Name the blood parasite species.
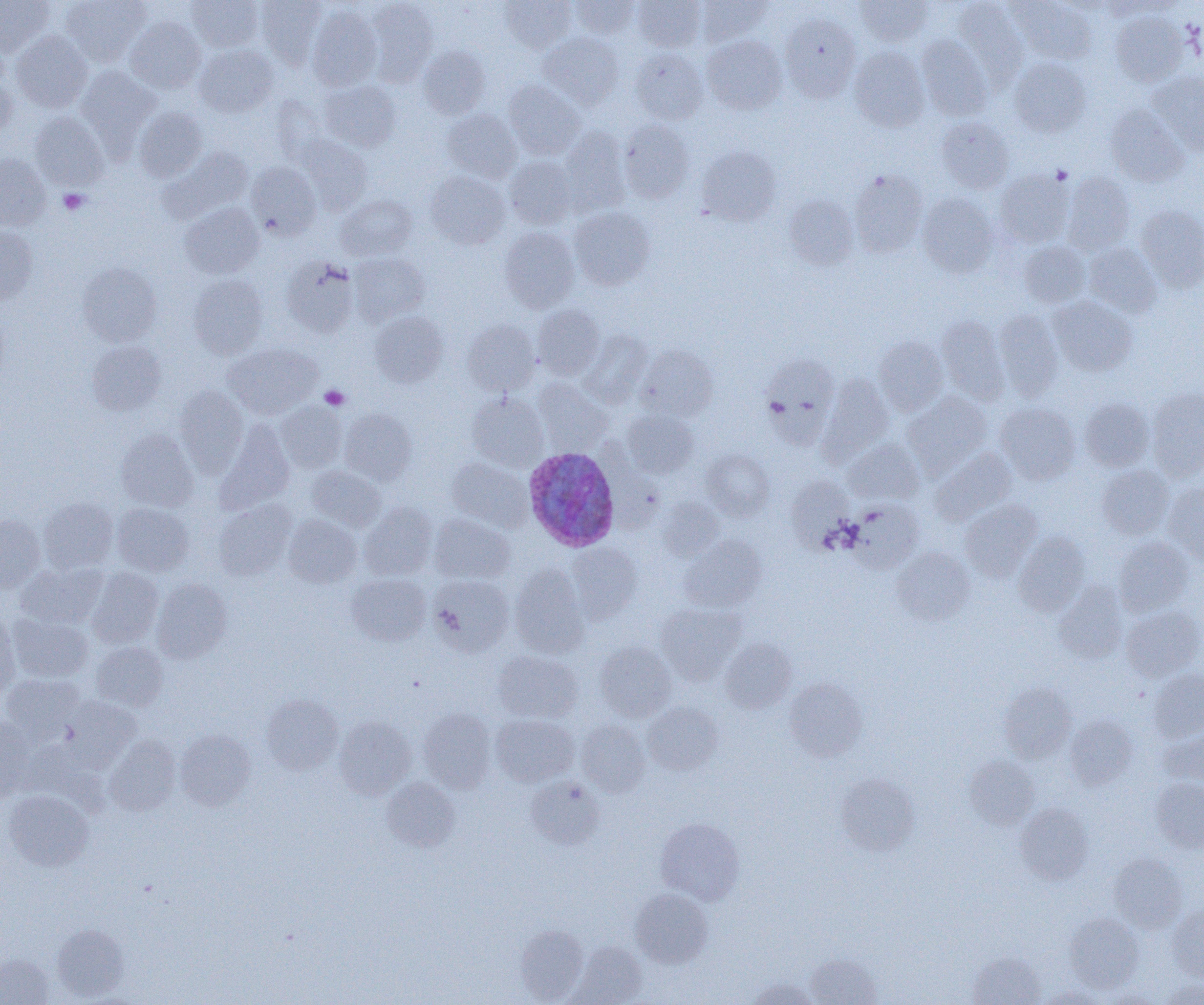
Plasmodium ovale.

Approximate bounding boxes as named x1/y1/x2/y2 corners in pixels. Platelet locations: (x1=59, y1=188, x2=89, y2=214), (x1=320, y1=385, x2=349, y2=410). Plasmodium ovale-infected red blood cell locations: (x1=523, y1=446, x2=620, y2=552). Uninfected red blood cell locations: (x1=0, y1=0, x2=54, y2=56), (x1=61, y1=0, x2=149, y2=65), (x1=187, y1=0, x2=263, y2=51), (x1=256, y1=0, x2=326, y2=69), (x1=366, y1=0, x2=438, y2=83), (x1=569, y1=0, x2=640, y2=39), (x1=632, y1=0, x2=705, y2=52), (x1=696, y1=0, x2=771, y2=46), (x1=856, y1=0, x2=931, y2=46), (x1=500, y1=1, x2=575, y2=52), (x1=954, y1=1, x2=1028, y2=86), (x1=1008, y1=1, x2=1096, y2=64), (x1=307, y1=5, x2=383, y2=91), (x1=1112, y1=11, x2=1189, y2=86), (x1=780, y1=14, x2=861, y2=102), (x1=125, y1=17, x2=206, y2=93), (x1=11, y1=30, x2=92, y2=112), (x1=539, y1=32, x2=623, y2=108), (x1=702, y1=35, x2=787, y2=114), (x1=916, y1=35, x2=992, y2=120), (x1=194, y1=44, x2=278, y2=117), (x1=418, y1=45, x2=490, y2=119), (x1=849, y1=47, x2=929, y2=132), (x1=630, y1=48, x2=708, y2=124), (x1=1009, y1=57, x2=1091, y2=137), (x1=76, y1=66, x2=160, y2=149), (x1=1147, y1=72, x2=1204, y2=156), (x1=0, y1=73, x2=17, y2=141), (x1=320, y1=80, x2=402, y2=151), (x1=503, y1=81, x2=586, y2=159), (x1=272, y1=95, x2=331, y2=166), (x1=1106, y1=105, x2=1189, y2=186), (x1=134, y1=107, x2=207, y2=181), (x1=443, y1=109, x2=521, y2=182), (x1=30, y1=112, x2=109, y2=190), (x1=936, y1=117, x2=1013, y2=193), (x1=619, y1=120, x2=694, y2=203), (x1=560, y1=127, x2=629, y2=214), (x1=296, y1=136, x2=372, y2=214), (x1=162, y1=146, x2=254, y2=223), (x1=696, y1=146, x2=780, y2=226), (x1=0, y1=154, x2=50, y2=231), (x1=505, y1=156, x2=578, y2=228), (x1=247, y1=162, x2=321, y2=239), (x1=849, y1=170, x2=927, y2=257), (x1=995, y1=170, x2=1074, y2=247), (x1=425, y1=171, x2=510, y2=249), (x1=1062, y1=172, x2=1135, y2=254), (x1=337, y1=194, x2=417, y2=260), (x1=918, y1=194, x2=998, y2=277), (x1=784, y1=195, x2=858, y2=270), (x1=181, y1=202, x2=264, y2=279), (x1=1136, y1=204, x2=1204, y2=291), (x1=569, y1=207, x2=655, y2=290), (x1=0, y1=226, x2=37, y2=304), (x1=499, y1=227, x2=579, y2=312), (x1=1019, y1=241, x2=1090, y2=309), (x1=1083, y1=243, x2=1162, y2=317), (x1=349, y1=253, x2=429, y2=325), (x1=280, y1=256, x2=359, y2=337), (x1=78, y1=262, x2=162, y2=346), (x1=188, y1=275, x2=267, y2=359), (x1=1049, y1=296, x2=1137, y2=376), (x1=533, y1=304, x2=605, y2=379), (x1=994, y1=310, x2=1063, y2=400), (x1=370, y1=311, x2=448, y2=387), (x1=937, y1=316, x2=1008, y2=402), (x1=462, y1=320, x2=541, y2=395), (x1=580, y1=330, x2=652, y2=408), (x1=873, y1=336, x2=948, y2=415), (x1=86, y1=340, x2=166, y2=415), (x1=223, y1=343, x2=322, y2=418), (x1=637, y1=345, x2=718, y2=421), (x1=762, y1=354, x2=840, y2=445), (x1=819, y1=375, x2=893, y2=461), (x1=534, y1=379, x2=611, y2=454), (x1=174, y1=386, x2=248, y2=475), (x1=1147, y1=389, x2=1204, y2=480), (x1=467, y1=392, x2=549, y2=471), (x1=904, y1=392, x2=992, y2=474), (x1=1080, y1=398, x2=1154, y2=471), (x1=276, y1=402, x2=347, y2=472), (x1=995, y1=403, x2=1081, y2=484), (x1=340, y1=408, x2=416, y2=485), (x1=622, y1=410, x2=698, y2=478), (x1=215, y1=422, x2=295, y2=513), (x1=116, y1=429, x2=198, y2=512), (x1=843, y1=439, x2=923, y2=504), (x1=931, y1=448, x2=1016, y2=526), (x1=702, y1=449, x2=774, y2=519), (x1=447, y1=458, x2=532, y2=531), (x1=1097, y1=465, x2=1174, y2=539), (x1=306, y1=466, x2=386, y2=531), (x1=786, y1=475, x2=851, y2=547), (x1=1164, y1=484, x2=1204, y2=565), (x1=38, y1=497, x2=118, y2=573), (x1=658, y1=497, x2=724, y2=561), (x1=214, y1=500, x2=297, y2=580), (x1=848, y1=500, x2=923, y2=571), (x1=961, y1=500, x2=1042, y2=581), (x1=360, y1=502, x2=437, y2=579), (x1=112, y1=503, x2=194, y2=575), (x1=284, y1=514, x2=362, y2=587), (x1=430, y1=514, x2=514, y2=584), (x1=0, y1=515, x2=46, y2=593), (x1=1013, y1=532, x2=1090, y2=616), (x1=680, y1=536, x2=766, y2=612), (x1=1114, y1=536, x2=1194, y2=616), (x1=568, y1=543, x2=642, y2=621), (x1=893, y1=547, x2=975, y2=625), (x1=16, y1=562, x2=109, y2=629), (x1=510, y1=565, x2=589, y2=656), (x1=86, y1=568, x2=163, y2=648), (x1=347, y1=573, x2=430, y2=646), (x1=430, y1=575, x2=513, y2=655), (x1=151, y1=578, x2=231, y2=662), (x1=1054, y1=582, x2=1127, y2=663), (x1=657, y1=602, x2=744, y2=683), (x1=1121, y1=605, x2=1204, y2=681), (x1=0, y1=612, x2=20, y2=698), (x1=7, y1=613, x2=93, y2=682), (x1=720, y1=638, x2=796, y2=713), (x1=91, y1=642, x2=168, y2=711), (x1=596, y1=642, x2=675, y2=721), (x1=492, y1=650, x2=582, y2=723), (x1=1148, y1=669, x2=1204, y2=741), (x1=1, y1=673, x2=85, y2=742), (x1=785, y1=678, x2=867, y2=761), (x1=999, y1=683, x2=1076, y2=762), (x1=261, y1=695, x2=343, y2=775), (x1=61, y1=696, x2=141, y2=771), (x1=643, y1=702, x2=723, y2=775), (x1=418, y1=708, x2=496, y2=792), (x1=491, y1=714, x2=578, y2=787), (x1=1065, y1=714, x2=1138, y2=789), (x1=0, y1=715, x2=36, y2=800), (x1=334, y1=717, x2=416, y2=800), (x1=576, y1=720, x2=650, y2=796), (x1=1159, y1=728, x2=1204, y2=787), (x1=175, y1=729, x2=256, y2=810), (x1=104, y1=736, x2=181, y2=815), (x1=964, y1=756, x2=1039, y2=829), (x1=835, y1=774, x2=919, y2=855), (x1=525, y1=776, x2=604, y2=849), (x1=382, y1=778, x2=460, y2=851), (x1=1150, y1=778, x2=1204, y2=852), (x1=3, y1=790, x2=94, y2=871), (x1=1016, y1=804, x2=1093, y2=884), (x1=655, y1=818, x2=745, y2=904), (x1=1109, y1=853, x2=1187, y2=932), (x1=630, y1=888, x2=713, y2=968), (x1=1168, y1=905, x2=1204, y2=982), (x1=1065, y1=912, x2=1143, y2=992), (x1=52, y1=924, x2=129, y2=1000), (x1=514, y1=924, x2=588, y2=1003), (x1=566, y1=941, x2=646, y2=1004), (x1=969, y1=952, x2=1045, y2=1005), (x1=0, y1=954, x2=53, y2=1004), (x1=807, y1=954, x2=881, y2=1005), (x1=747, y1=978, x2=818, y2=1005), (x1=1161, y1=980, x2=1204, y2=1004), (x1=1038, y1=985, x2=1109, y2=1004). One field of a larger specimen. Image is 1204×1005 pixels. 1000x magnification. Thin blood smear. Optical microscopy.